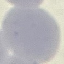

{
  "malaria_status": "uninfected",
  "preparation": "thin blood smear",
  "capture": "smartphone camera at the microscope eyepiece",
  "stain": "Giemsa",
  "image_type": "cell patch, automatically extracted from a larger field of view and resized to 64 × 64 pixels"
}